State which cell type is depicted.
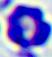

This is a leukocyte.

Summary:
  - Modality: photomicrograph
  - Magnification: 400x